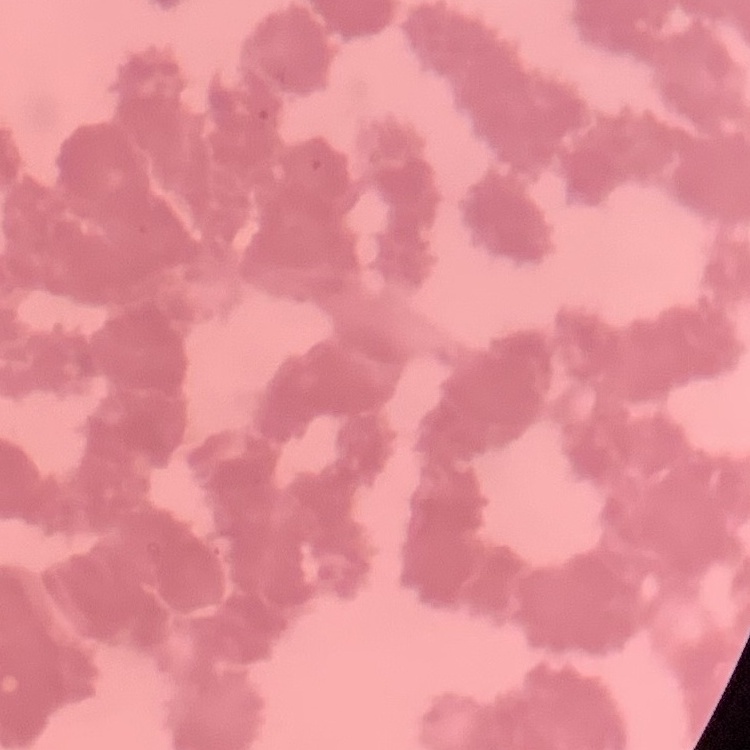

{
  "red_blood_cell_morphology": "rouleaux formation",
  "stain": "Field's or Giemsa",
  "preparation": "thin blood film",
  "image_type": "square crop of a larger photomicrograph"
}